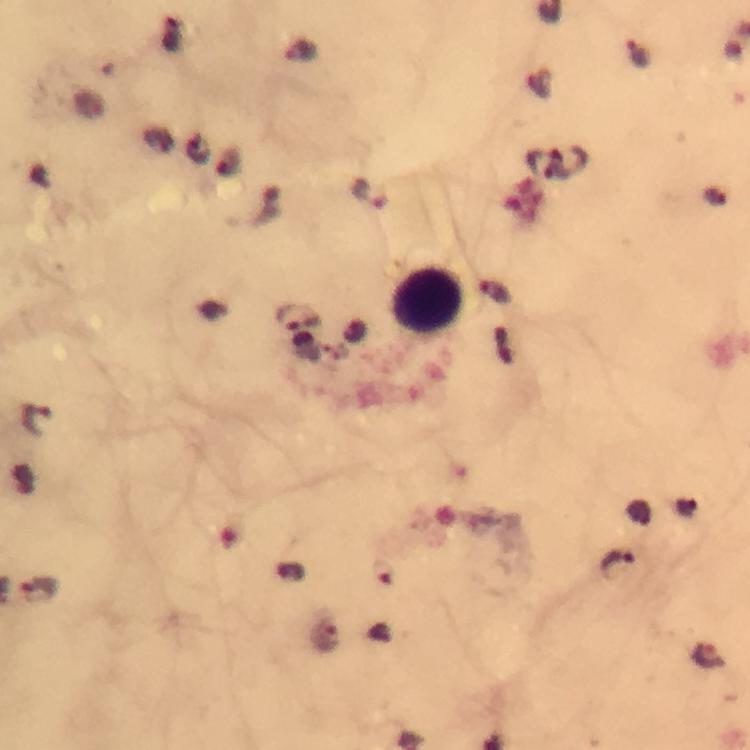
context = from a malaria diagnostic workup
image size = 750×750 pixels
stain = Giemsa
preparation = thick blood smear
leukocyte locations = approximate centers as [x, y] in pixels: [429, 299]
immersion oil = applied
capture = smartphone photograph through a microscope
magnification = 100x
cropped from = one field of view
Plasmodium parasite locations = approximate centers as [x, y] in pixels: [300, 50], [638, 54], [369, 194], [496, 293], [300, 317], [36, 419], [618, 563], [38, 590], [326, 638], [708, 656]